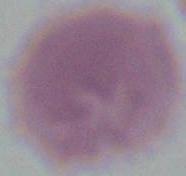

modality: micrograph
magnification: 1000x
identification: erythrocyte